Name the blood parasite species.
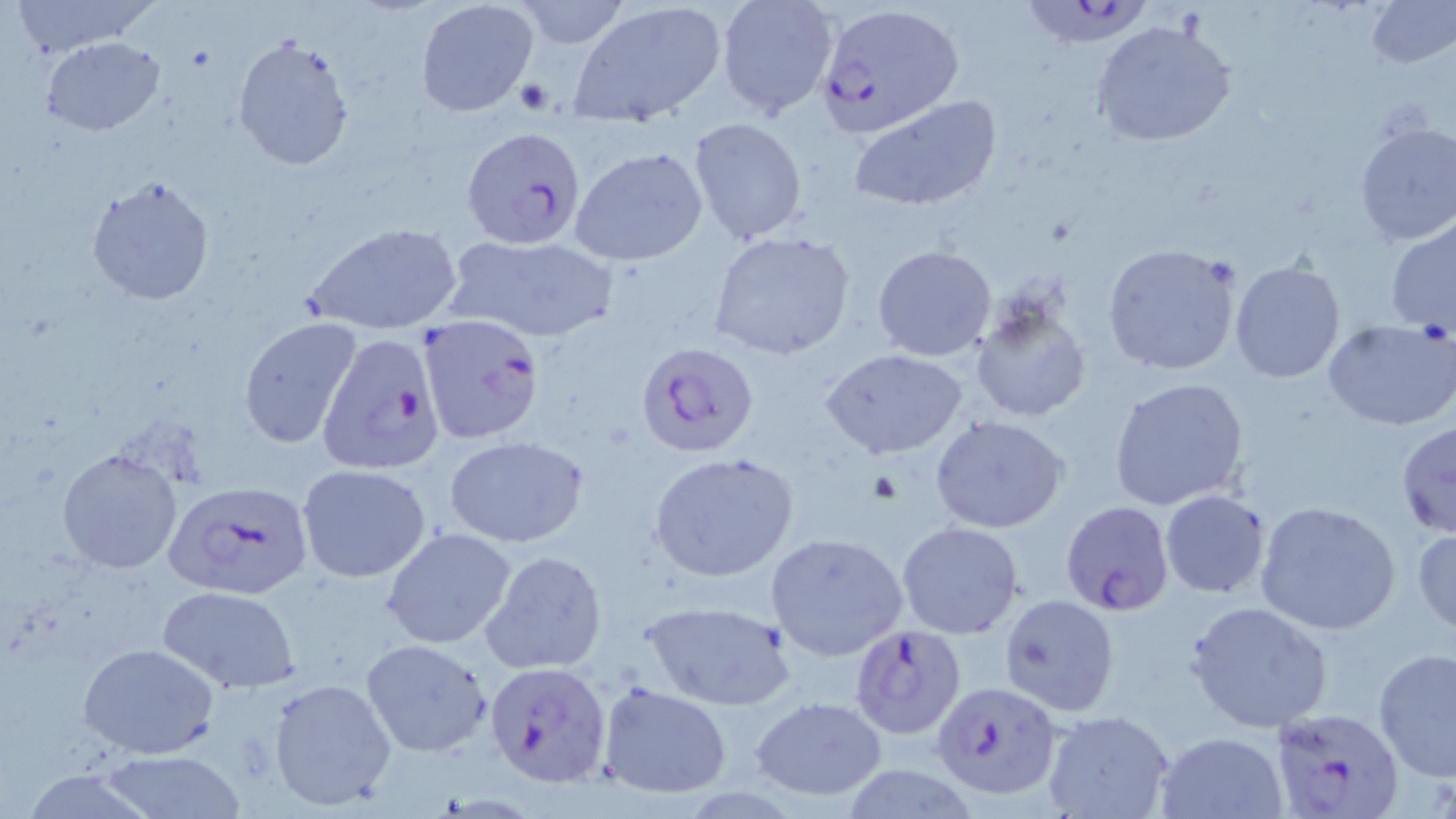
Plasmodium falciparum.

Approximate bounding boxes as [x1, y1, x2, y2] in pixels. Plasmodium falciparum-infected red blood cell locations: [1013, 0, 1162, 51], [814, 4, 964, 138], [456, 127, 586, 248], [418, 314, 547, 445], [316, 332, 446, 476], [636, 340, 760, 458], [161, 482, 313, 602], [1060, 500, 1176, 618], [848, 624, 968, 741], [485, 661, 612, 788], [930, 684, 1060, 805], [1268, 706, 1406, 816]. Uninfected red blood cell locations: [10, 0, 162, 58], [512, 0, 634, 51], [716, 0, 841, 119], [569, 1, 728, 124], [1365, 1, 1455, 70], [415, 2, 538, 116], [1091, 19, 1239, 147], [232, 34, 356, 172], [43, 37, 164, 135], [846, 94, 1003, 214], [689, 118, 810, 246], [1352, 120, 1456, 246], [569, 146, 707, 268], [86, 175, 216, 305], [1385, 217, 1456, 336], [301, 220, 466, 332], [710, 231, 857, 361], [449, 234, 621, 342], [1102, 243, 1243, 376], [872, 245, 997, 362], [1227, 260, 1348, 384], [969, 296, 1092, 424], [1322, 317, 1456, 432], [236, 318, 361, 450], [822, 349, 968, 459], [1108, 377, 1251, 512], [932, 417, 1068, 533], [1395, 419, 1456, 539], [443, 435, 590, 548], [58, 448, 183, 573], [648, 452, 799, 584], [298, 465, 431, 583], [1160, 490, 1271, 597], [1254, 501, 1402, 635], [898, 521, 1022, 639], [1411, 525, 1456, 636], [380, 527, 518, 650], [765, 532, 908, 661], [480, 550, 609, 675], [156, 585, 300, 695], [998, 594, 1120, 717], [640, 600, 795, 712], [1186, 600, 1335, 734], [360, 639, 493, 758], [77, 642, 222, 759], [1373, 648, 1456, 779], [267, 677, 399, 813], [598, 682, 733, 798], [752, 696, 888, 800], [1041, 711, 1173, 819], [1156, 730, 1287, 818], [103, 749, 247, 817]. Platelet locations: [514, 76, 554, 115]. Image is 1456×819 pixels. Light microscopy. Thin blood film. May-Grünwald-Giemsa-stained preparation. Captured at 1000x magnification. Single field of view.